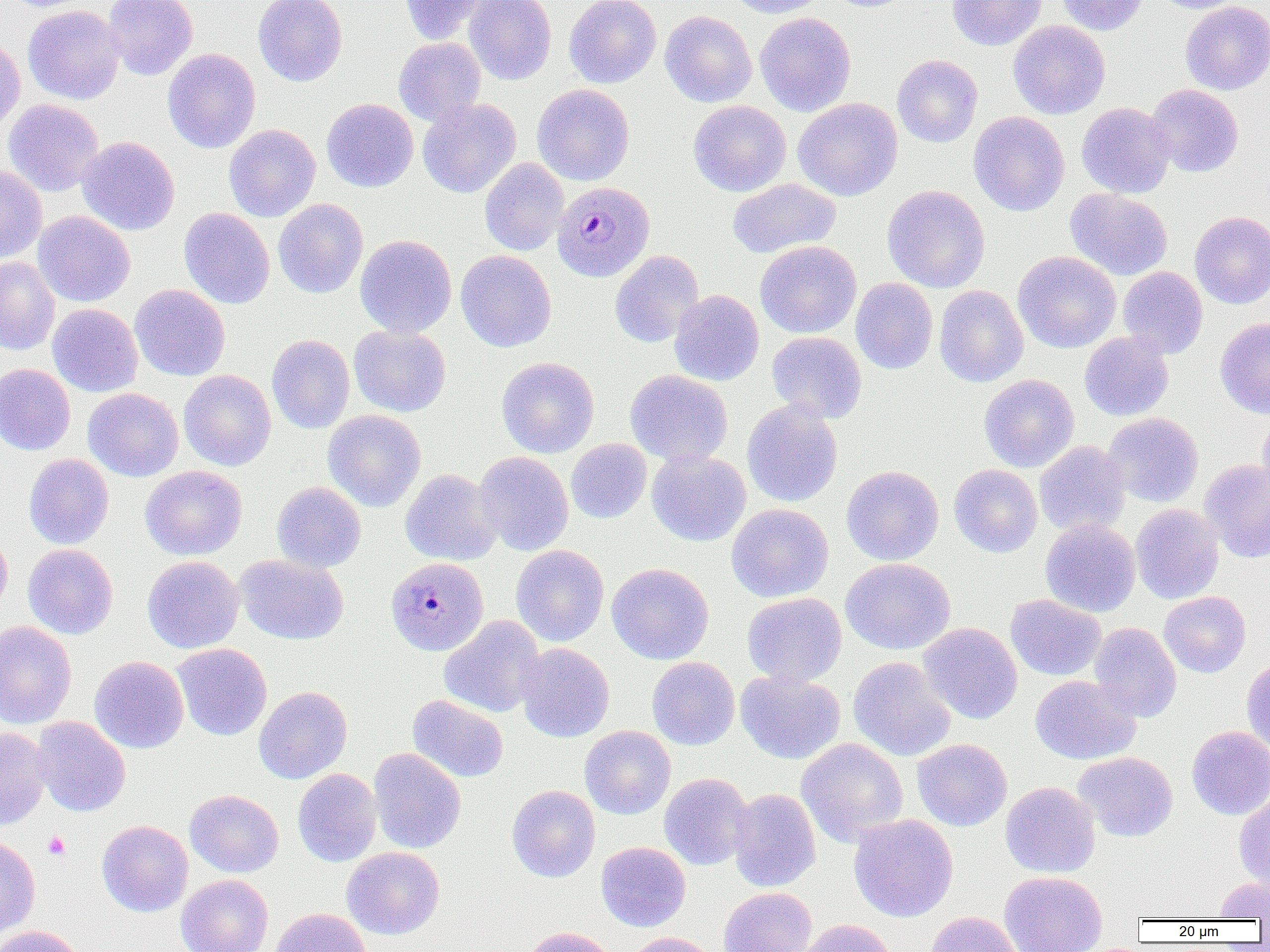

slide-level diagnosis = Plasmodium malariae
modality = optical microscopy
Plasmodium malariae-infected red blood cell locations = approximate bounding boxes as named x1/y1/x2/y2 corners in pixels: (x1=552, y1=182, x2=655, y2=281), (x1=384, y1=555, x2=487, y2=654)
magnification = 1000x
image size = 1270×952 pixels
field of view = one of a larger specimen
preparation = thin blood film
uninfected red blood cell locations = approximate bounding boxes as named x1/y1/x2/y2 corners in pixels: (x1=103, y1=0, x2=198, y2=80), (x1=253, y1=0, x2=347, y2=86), (x1=400, y1=0, x2=490, y2=44), (x1=464, y1=0, x2=556, y2=85), (x1=564, y1=0, x2=661, y2=88), (x1=725, y1=0, x2=828, y2=18), (x1=823, y1=0, x2=918, y2=12), (x1=947, y1=0, x2=1047, y2=51), (x1=1056, y1=0, x2=1149, y2=35), (x1=1152, y1=0, x2=1247, y2=13), (x1=1180, y1=1, x2=1270, y2=95), (x1=23, y1=4, x2=126, y2=105), (x1=660, y1=10, x2=757, y2=108), (x1=754, y1=12, x2=856, y2=116), (x1=1008, y1=20, x2=1110, y2=120), (x1=0, y1=35, x2=25, y2=134), (x1=393, y1=37, x2=486, y2=127), (x1=162, y1=48, x2=261, y2=153), (x1=892, y1=55, x2=982, y2=148), (x1=532, y1=83, x2=635, y2=186), (x1=1146, y1=84, x2=1243, y2=177), (x1=418, y1=97, x2=521, y2=198), (x1=321, y1=98, x2=418, y2=192), (x1=793, y1=98, x2=903, y2=201), (x1=4, y1=99, x2=104, y2=196), (x1=688, y1=100, x2=791, y2=196), (x1=1076, y1=102, x2=1176, y2=198), (x1=968, y1=111, x2=1070, y2=216), (x1=224, y1=124, x2=321, y2=222), (x1=77, y1=136, x2=180, y2=235), (x1=479, y1=158, x2=569, y2=255), (x1=0, y1=165, x2=47, y2=264), (x1=727, y1=178, x2=841, y2=258), (x1=882, y1=185, x2=990, y2=292), (x1=1065, y1=188, x2=1173, y2=280), (x1=273, y1=198, x2=368, y2=298), (x1=179, y1=208, x2=275, y2=309), (x1=33, y1=211, x2=135, y2=307), (x1=1189, y1=211, x2=1270, y2=309), (x1=355, y1=234, x2=457, y2=338), (x1=755, y1=240, x2=861, y2=338), (x1=456, y1=250, x2=556, y2=352), (x1=609, y1=250, x2=704, y2=348), (x1=1012, y1=251, x2=1121, y2=353), (x1=0, y1=257, x2=60, y2=355), (x1=1118, y1=266, x2=1208, y2=359), (x1=850, y1=278, x2=938, y2=374), (x1=130, y1=285, x2=230, y2=381), (x1=934, y1=285, x2=1028, y2=387), (x1=670, y1=290, x2=764, y2=386), (x1=47, y1=303, x2=143, y2=397), (x1=1215, y1=318, x2=1270, y2=419), (x1=348, y1=324, x2=451, y2=417), (x1=767, y1=331, x2=867, y2=422), (x1=1079, y1=332, x2=1173, y2=421), (x1=266, y1=334, x2=355, y2=434), (x1=496, y1=357, x2=599, y2=458), (x1=0, y1=364, x2=75, y2=455), (x1=178, y1=369, x2=276, y2=471), (x1=624, y1=370, x2=733, y2=467), (x1=979, y1=374, x2=1079, y2=472), (x1=83, y1=388, x2=183, y2=481), (x1=742, y1=400, x2=843, y2=507), (x1=323, y1=410, x2=426, y2=511), (x1=1257, y1=412, x2=1270, y2=503), (x1=1102, y1=413, x2=1203, y2=507), (x1=566, y1=438, x2=652, y2=523), (x1=1034, y1=440, x2=1130, y2=536), (x1=647, y1=450, x2=751, y2=546), (x1=474, y1=451, x2=574, y2=556), (x1=24, y1=454, x2=114, y2=549), (x1=1200, y1=459, x2=1270, y2=562), (x1=949, y1=464, x2=1043, y2=557), (x1=140, y1=465, x2=247, y2=560), (x1=841, y1=465, x2=944, y2=565), (x1=400, y1=469, x2=502, y2=566), (x1=272, y1=481, x2=366, y2=572), (x1=726, y1=503, x2=834, y2=602), (x1=1130, y1=504, x2=1224, y2=604), (x1=1041, y1=518, x2=1140, y2=617), (x1=0, y1=531, x2=12, y2=618), (x1=22, y1=544, x2=118, y2=639), (x1=511, y1=544, x2=609, y2=647), (x1=234, y1=554, x2=349, y2=645), (x1=142, y1=555, x2=244, y2=653), (x1=840, y1=558, x2=956, y2=655), (x1=607, y1=563, x2=714, y2=665), (x1=1159, y1=591, x2=1251, y2=678), (x1=742, y1=592, x2=847, y2=686), (x1=1005, y1=594, x2=1106, y2=681), (x1=439, y1=615, x2=546, y2=718), (x1=0, y1=621, x2=77, y2=729), (x1=917, y1=622, x2=1023, y2=724), (x1=1089, y1=622, x2=1182, y2=722), (x1=515, y1=642, x2=615, y2=742), (x1=171, y1=643, x2=272, y2=741), (x1=90, y1=656, x2=189, y2=753), (x1=647, y1=657, x2=740, y2=750), (x1=848, y1=657, x2=956, y2=762), (x1=1241, y1=657, x2=1270, y2=752), (x1=735, y1=671, x2=846, y2=764), (x1=1030, y1=675, x2=1140, y2=764), (x1=253, y1=686, x2=352, y2=784), (x1=408, y1=694, x2=509, y2=783), (x1=31, y1=717, x2=131, y2=816), (x1=580, y1=725, x2=676, y2=819), (x1=1186, y1=726, x2=1270, y2=819), (x1=0, y1=727, x2=52, y2=830), (x1=796, y1=738, x2=909, y2=846), (x1=912, y1=738, x2=1012, y2=831), (x1=368, y1=748, x2=466, y2=853), (x1=1073, y1=752, x2=1178, y2=842), (x1=293, y1=768, x2=382, y2=866), (x1=659, y1=773, x2=754, y2=870), (x1=1000, y1=781, x2=1100, y2=878), (x1=507, y1=785, x2=601, y2=883), (x1=728, y1=788, x2=821, y2=892), (x1=185, y1=789, x2=284, y2=877), (x1=1234, y1=790, x2=1270, y2=891), (x1=848, y1=814, x2=958, y2=922), (x1=97, y1=820, x2=193, y2=917), (x1=0, y1=835, x2=40, y2=940), (x1=596, y1=841, x2=691, y2=931), (x1=342, y1=847, x2=444, y2=939), (x1=999, y1=871, x2=1108, y2=952), (x1=176, y1=874, x2=273, y2=952), (x1=1215, y1=877, x2=1270, y2=920), (x1=718, y1=887, x2=818, y2=952), (x1=270, y1=907, x2=372, y2=952), (x1=925, y1=911, x2=1024, y2=952), (x1=798, y1=919, x2=898, y2=952), (x1=1, y1=925, x2=85, y2=952), (x1=522, y1=927, x2=617, y2=952), (x1=623, y1=932, x2=720, y2=952)
platelet locations = approximate bounding boxes as named x1/y1/x2/y2 corners in pixels: (x1=43, y1=831, x2=70, y2=860)